Assess for Plasmodium parasites.
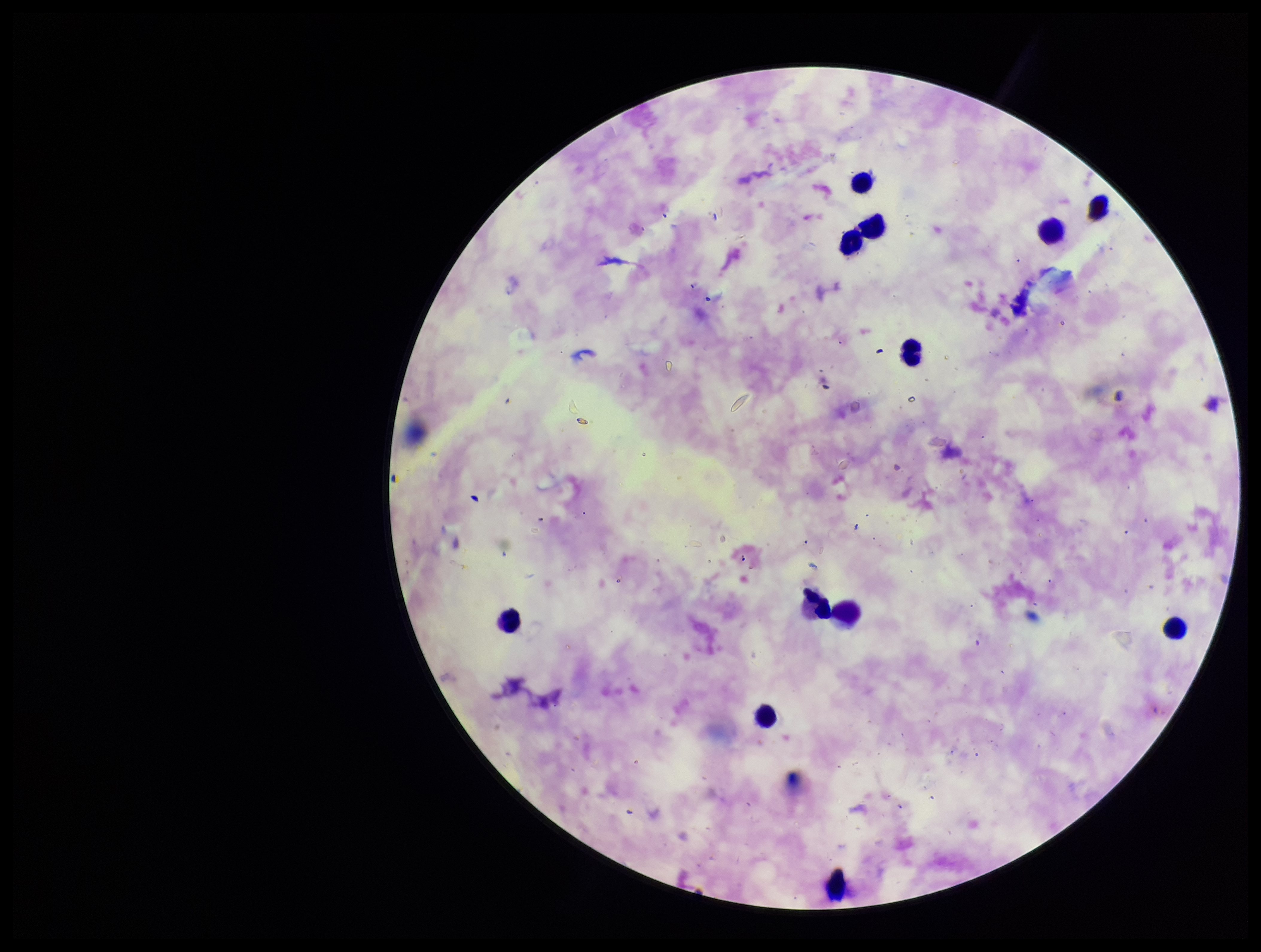
None detected.

Summary:
  - Image size: 1261×952 pixels
  - Field of view: one from this slide
  - Stain: Giemsa
  - Patient malaria status: positive
  - Preparation: thick blood smear
  - Species reported for this patient: Plasmodium falciparum
  - Leukocyte count: 12
  - Capture: smartphone photograph through the microscope eyepiece
  - Parasite count: 0